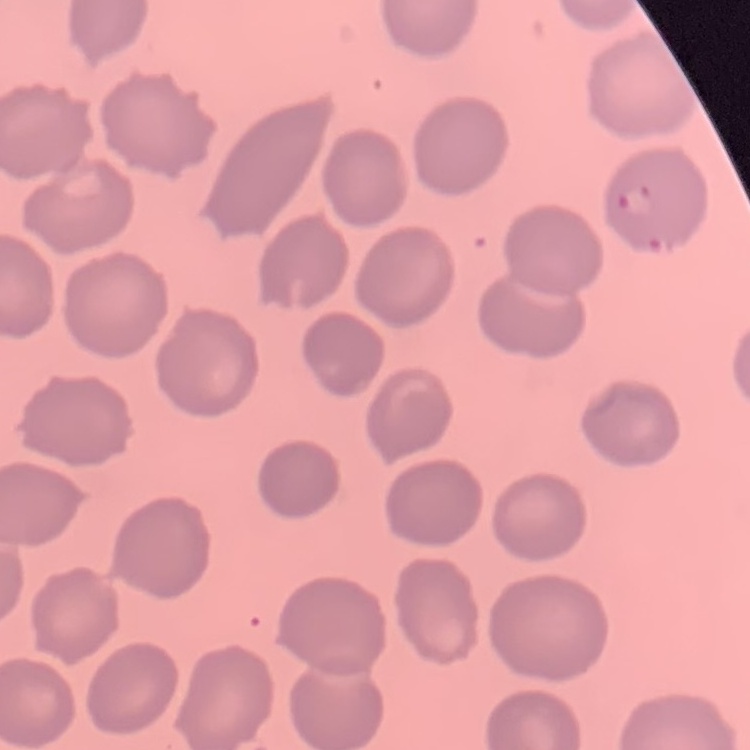
Summary:
  - Erythrocyte morphology: no rouleaux formation
  - Image type: one tile cut from a larger photomicrograph
  - Preparation: thin peripheral smear
  - Stain: Field's or Giemsa